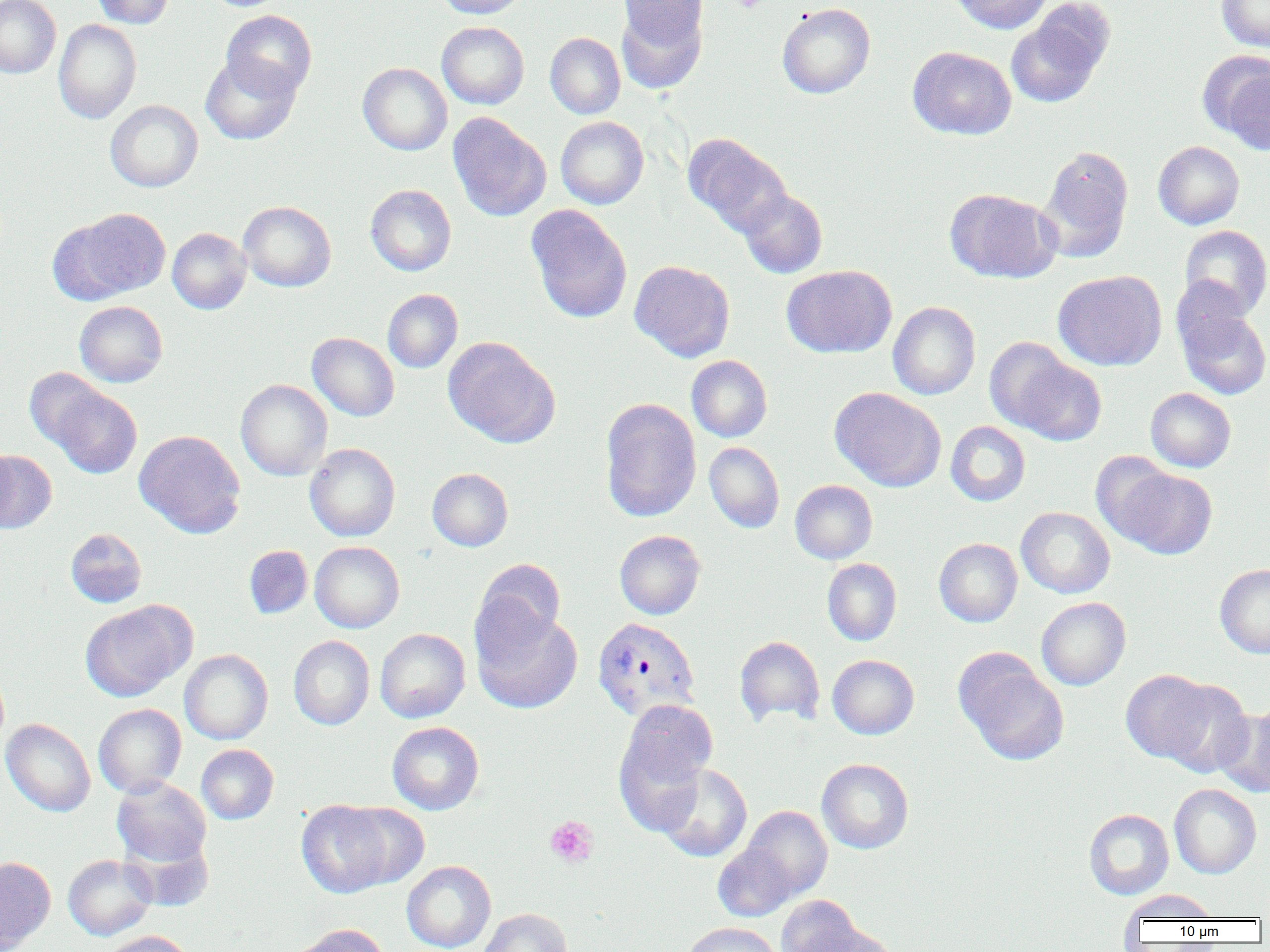
Summary:
  - Coordinate format: approximate bounding boxes as [x1, y1, x2, y2] in pixels
  - Platelet locations: [728, 0, 770, 12], [545, 816, 598, 867]
  - Uninfected red blood cell locations: [0, 0, 61, 79], [91, 0, 177, 28], [435, 0, 528, 18], [950, 0, 1052, 34], [1216, 0, 1270, 53], [616, 2, 708, 91], [777, 3, 875, 99], [1005, 5, 1113, 108], [221, 10, 317, 100], [53, 19, 141, 124], [437, 22, 529, 109], [545, 32, 625, 119], [908, 46, 1016, 140], [1200, 50, 1270, 150], [201, 54, 301, 145], [358, 63, 452, 155], [105, 100, 203, 192], [448, 113, 551, 222], [556, 116, 648, 209], [685, 134, 791, 236], [1153, 141, 1244, 229], [1039, 146, 1134, 261], [365, 184, 456, 276], [945, 188, 1060, 283], [738, 189, 827, 278], [238, 201, 336, 292], [526, 205, 632, 324], [54, 208, 171, 303], [1179, 225, 1270, 319], [167, 228, 251, 314], [630, 260, 735, 362], [782, 265, 897, 358], [1053, 270, 1166, 370], [383, 289, 463, 373], [1175, 298, 1270, 401], [74, 301, 168, 387], [888, 302, 980, 400], [307, 332, 400, 421], [443, 337, 560, 448], [984, 337, 1078, 434], [686, 355, 772, 442], [1012, 355, 1107, 446], [24, 367, 109, 452], [235, 379, 332, 480], [49, 386, 142, 478], [830, 387, 946, 491], [1145, 388, 1236, 472], [599, 398, 702, 522], [945, 421, 1030, 506], [134, 429, 246, 538], [0, 441, 16, 530], [704, 442, 785, 533], [304, 443, 400, 541], [0, 450, 57, 533], [1090, 451, 1179, 544], [1116, 467, 1217, 560], [427, 468, 513, 551], [790, 480, 878, 564], [1016, 507, 1115, 598], [65, 528, 147, 608], [614, 530, 706, 620], [934, 538, 1022, 627], [309, 541, 404, 633], [243, 545, 313, 619], [474, 558, 567, 649], [822, 558, 902, 646], [1215, 564, 1270, 658], [1036, 597, 1131, 690], [80, 600, 194, 701], [471, 605, 583, 715], [375, 628, 470, 722], [289, 635, 375, 730], [734, 635, 825, 727], [179, 649, 273, 744], [955, 651, 1070, 766], [827, 654, 919, 739], [1121, 669, 1215, 764], [1158, 680, 1254, 778], [615, 698, 717, 817], [93, 704, 186, 797], [1215, 705, 1270, 797], [1, 718, 96, 816], [387, 721, 484, 814], [197, 744, 279, 824], [816, 758, 914, 854], [655, 763, 753, 862], [112, 777, 212, 869], [1169, 784, 1262, 879], [296, 799, 400, 898], [339, 803, 429, 890], [742, 806, 833, 899], [1083, 808, 1174, 900], [713, 843, 797, 921], [63, 854, 156, 940], [0, 856, 56, 951], [401, 860, 496, 952], [1121, 889, 1220, 922], [776, 894, 863, 952], [478, 908, 573, 952], [681, 921, 782, 952], [290, 924, 390, 952], [801, 925, 902, 952], [100, 930, 195, 952]
  - Plasmodium vivax-infected red blood cell locations: [591, 616, 700, 722]
  - Slide-level diagnosis: Plasmodium vivax
  - Field of view: single
  - Image size: 1270×952 pixels
  - Preparation: thin blood film
  - Modality: light microscopy
  - Magnification: 1000x